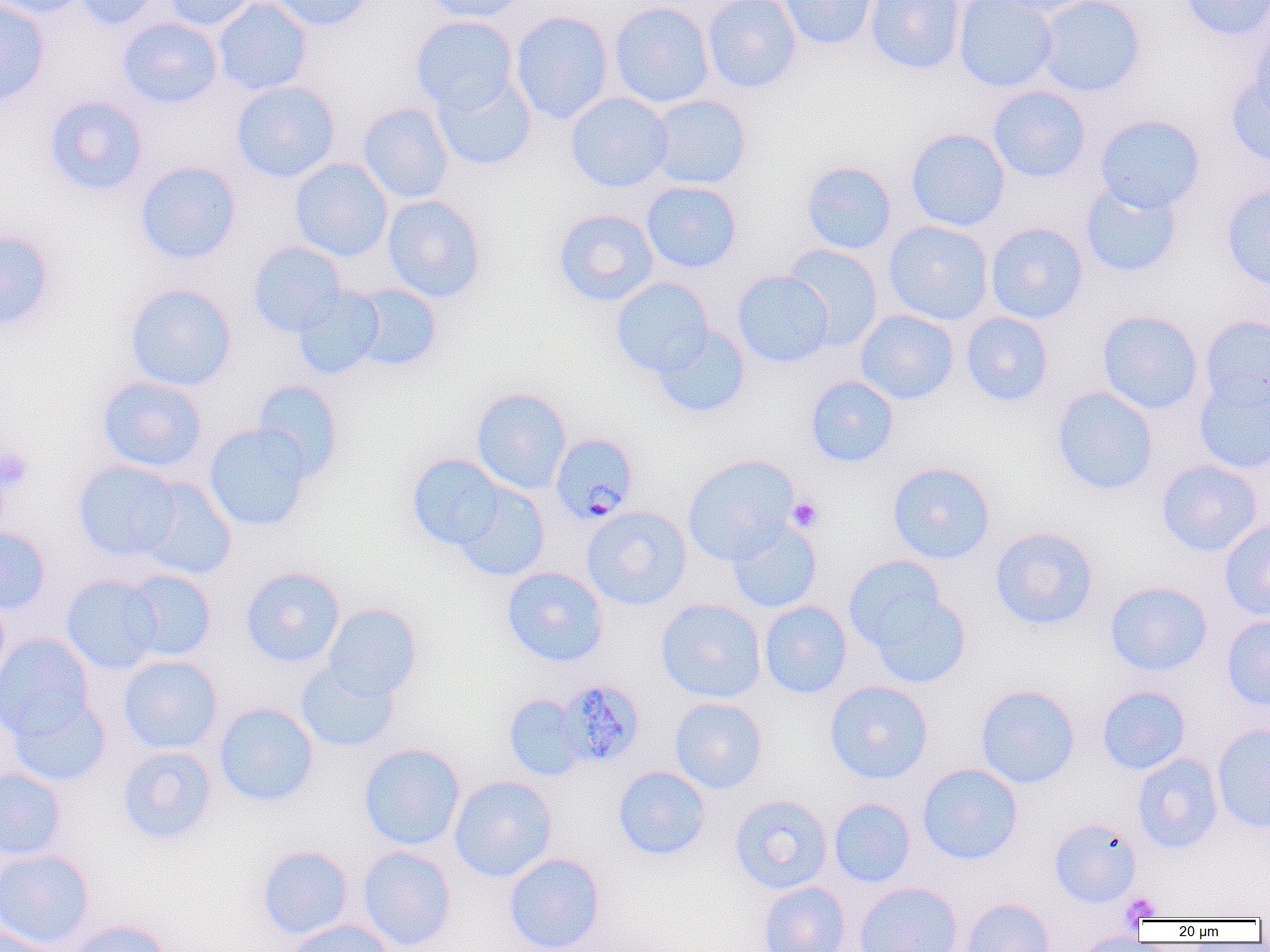
slide_level_diagnosis: Plasmodium malariae
modality: optical microscopy
field_of_view: single
plasmodium_malariae_infected_red_blood_cell_locations: 'approximate bounding boxes as (x1,y1)-(x2,y2) corner pairs in pixels: (550,432)-(639,525), (560,685)-(650,775)'
preparation: thin blood smear
uninfected_red_blood_cell_locations: 'approximate bounding boxes as (x1,y1)-(x2,y2) corner pairs in pixels: (0,0)-(50,107), (0,0)-(89,19), (72,0)-(159,30), (162,0)-(258,32), (212,0)-(314,96), (268,0)-(375,31), (421,0)-(527,22), (701,0)-(802,94), (778,0)-(877,51), (863,0)-(966,76), (953,0)-(1058,92), (989,0)-(1099,18), (1034,0)-(1146,98), (1179,0)-(1269,42), (608,2)-(715,109), (509,11)-(614,124), (409,15)-(519,115), (116,17)-(224,109), (1249,19)-(1270,123), (432,73)-(536,171), (1225,75)-(1270,167), (231,81)-(340,183), (988,85)-(1091,183), (565,92)-(674,193), (646,94)-(752,190), (43,96)-(149,196), (357,103)-(454,204), (1094,114)-(1205,213), (905,128)-(1011,232), (289,158)-(393,262), (135,161)-(241,265), (800,161)-(897,255), (1079,179)-(1183,278), (641,181)-(742,273), (1219,185)-(1270,290), (382,194)-(486,303), (553,209)-(659,306), (882,220)-(994,326), (985,222)-(1087,324), (0,228)-(56,331), (247,241)-(346,337), (782,244)-(884,350), (732,270)-(834,367), (610,277)-(715,377), (124,283)-(237,392), (349,284)-(444,372), (292,287)-(385,380), (855,309)-(959,405), (1096,310)-(1204,415), (960,311)-(1053,407), (1199,315)-(1270,412), (651,324)-(751,419), (1193,371)-(1270,475), (96,375)-(208,474), (805,375)-(899,468), (250,380)-(344,482), (1051,386)-(1158,496), (471,387)-(571,494), (203,423)-(313,531), (406,454)-(507,551), (682,454)-(799,564), (72,459)-(184,563), (1156,459)-(1263,557), (886,461)-(996,564), (135,478)-(236,580), (452,481)-(551,582), (581,506)-(692,611), (726,519)-(823,613), (1218,519)-(1270,621), (0,527)-(51,615), (989,527)-(1098,631), (845,559)-(969,684), (501,566)-(609,667), (239,567)-(346,668), (121,569)-(217,662), (60,575)-(164,674), (1104,581)-(1213,677), (0,593)-(10,693), (655,599)-(767,703), (758,601)-(853,699), (322,603)-(422,701), (1221,614)-(1270,712), (0,632)-(95,740), (118,655)-(222,755), (296,660)-(401,753), (823,680)-(933,784), (975,684)-(1081,789), (1097,685)-(1190,775), (7,693)-(111,787), (503,694)-(588,782), (669,697)-(768,794), (213,702)-(319,807), (1211,723)-(1270,833), (358,743)-(465,851), (117,745)-(217,845), (1132,753)-(1223,854), (917,763)-(1023,865), (613,765)-(711,861), (0,768)-(66,862), (449,775)-(558,882), (729,794)-(833,894), (828,797)-(916,888), (1048,818)-(1142,908), (256,845)-(355,941), (356,846)-(457,951), (0,848)-(95,951), (503,852)-(606,952), (758,880)-(851,952), (854,882)-(964,952), (960,897)-(1056,952), (65,919)-(175,952), (283,919)-(395,952), (0,928)-(66,952), (1072,933)-(1158,951)'
image_size: 1270×952 pixels
platelet_locations: 'approximate bounding boxes as (x1,y1)-(x2,y2) corner pairs in pixels: (0,444)-(33,494), (787,497)-(823,532), (1121,891)-(1162,923)'
magnification: 1000x